Point out each Plasmodium parasite and each leukocyte.
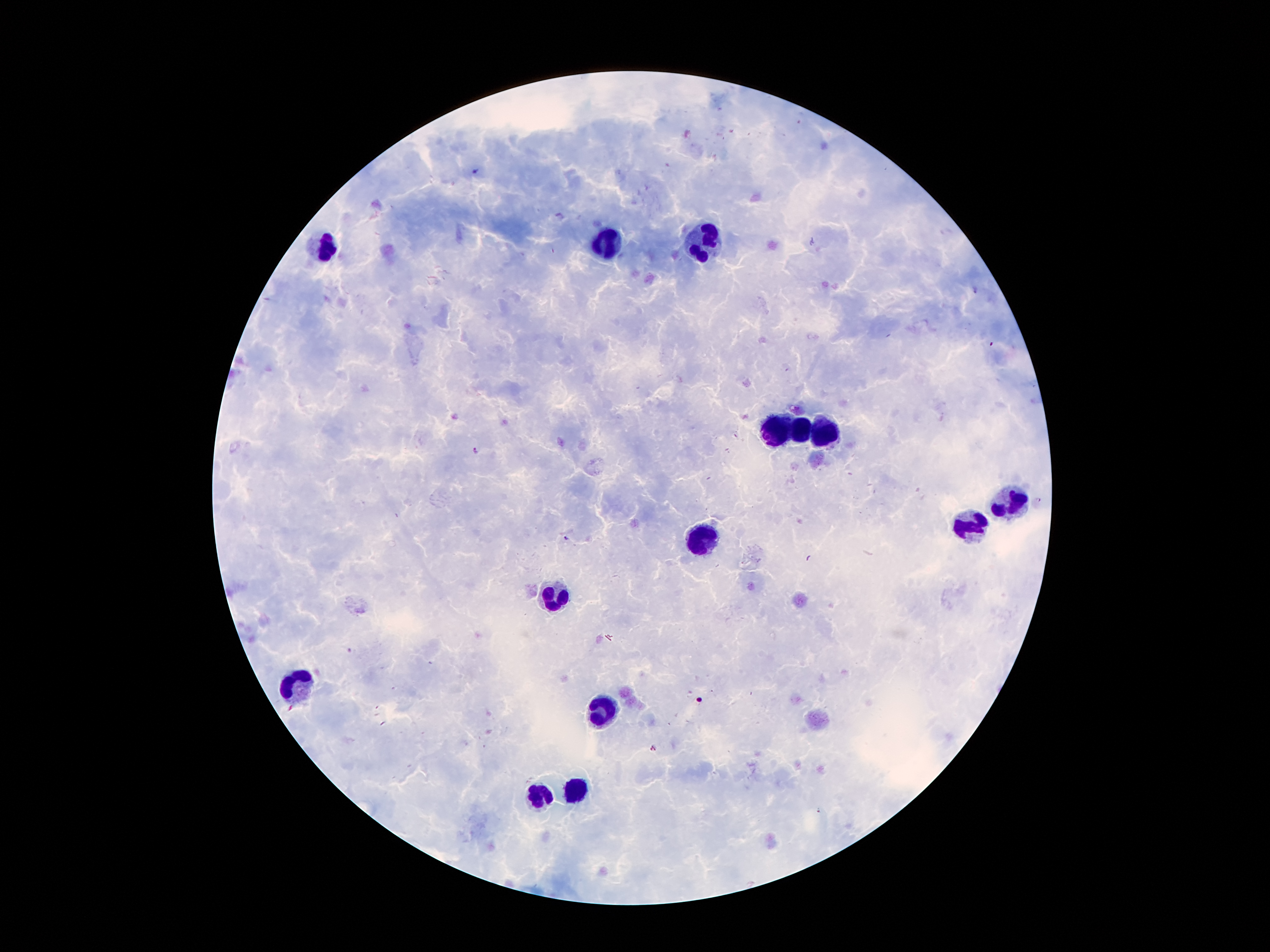
Approximate object centers, in pixels from the top-left corner.
Plasmodium parasites: (x=477, y=172), (x=977, y=292), (x=476, y=451), (x=1038, y=499), (x=565, y=537), (x=653, y=748).
Leukocytes: (x=704, y=241), (x=323, y=244), (x=609, y=247), (x=825, y=428), (x=778, y=431), (x=801, y=434), (x=1006, y=498), (x=967, y=527), (x=702, y=540), (x=553, y=596), (x=298, y=684), (x=604, y=712), (x=576, y=790), (x=538, y=796).

Image is 1270×952 pixels. Giemsa stain. Smartphone photograph taken through the microscope eyepiece. Thick blood smear. Patient malaria status: infected with Plasmodium falciparum. 100x magnification. Single field of view.